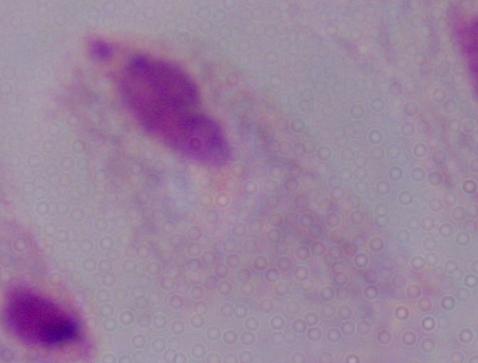

magnification: 1000x
identification: trichomonad
modality: micrograph